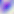

Summary:
  - Magnification: 400x
  - Modality: micrograph
  - Identification: Toxoplasma gondii